Locate every Plasmodium falciparum-infected red blood cell.
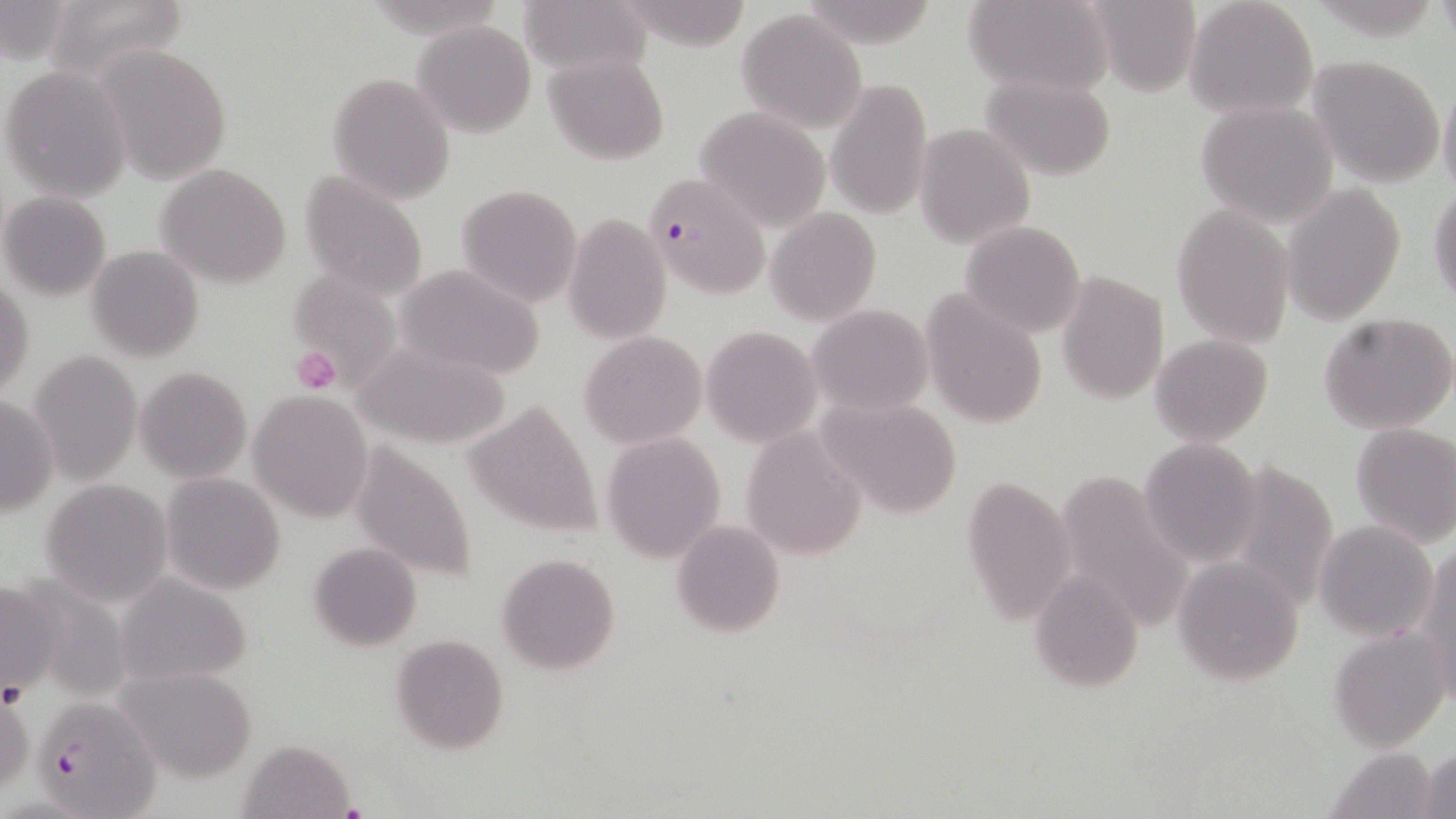

Approximate bounding boxes as (x1,y1)-(x2,y2) corner pairs in pixels.
Plasmodium falciparum-infected red blood cells: (642,174)-(771,300), (31,702)-(160,819).

Uninfected red blood cell locations: (41,0)-(193,84), (519,0)-(653,80), (962,0)-(1111,96), (1080,1)-(1204,96), (1184,1)-(1317,122), (1,2)-(74,64), (737,7)-(869,135), (413,19)-(536,139), (93,42)-(236,184), (546,53)-(670,164), (1306,54)-(1445,186), (1,65)-(133,202), (980,71)-(1116,181), (326,72)-(456,206), (827,76)-(933,222), (1437,80)-(1456,199), (1195,99)-(1340,227), (692,107)-(833,232), (914,124)-(1036,249), (156,162)-(295,289), (296,170)-(431,306), (1428,181)-(1456,307), (455,183)-(583,309), (1280,184)-(1407,326), (1,191)-(111,302), (1171,203)-(1296,347), (765,207)-(882,325), (562,213)-(672,345), (959,220)-(1087,336), (85,245)-(206,363), (395,265)-(548,381), (289,269)-(403,388), (1055,271)-(1169,405), (0,277)-(34,401), (921,290)-(1051,431), (806,304)-(933,417), (1318,312)-(1456,435), (701,326)-(821,446), (579,331)-(708,447), (1149,334)-(1273,445), (349,338)-(512,449), (27,351)-(142,485), (134,366)-(252,483), (249,389)-(374,522), (1,392)-(57,521), (816,396)-(964,520), (464,399)-(602,538), (1350,422)-(1456,548), (739,427)-(869,560), (601,432)-(726,563), (348,438)-(479,585), (1138,438)-(1262,566), (1051,467)-(1192,634), (161,473)-(286,594), (958,473)-(1077,627), (40,479)-(173,606), (670,520)-(786,638), (1313,520)-(1438,640), (308,541)-(424,652), (1417,542)-(1456,700), (495,553)-(622,676), (1171,553)-(1306,688), (1029,571)-(1144,694), (0,574)-(60,701), (114,575)-(255,688), (1328,627)-(1451,751), (390,633)-(509,753), (116,664)-(260,783), (0,687)-(34,797), (234,737)-(357,818), (1419,746)-(1455,818), (1325,747)-(1439,819). Platelet locations: (292,346)-(340,393). Slide-level diagnosis: Plasmodium falciparum. Image is 1456×819 pixels. Light microscopy. May-Grünwald-Giemsa stain. 1000x magnification. Single field of view. Thin blood film.